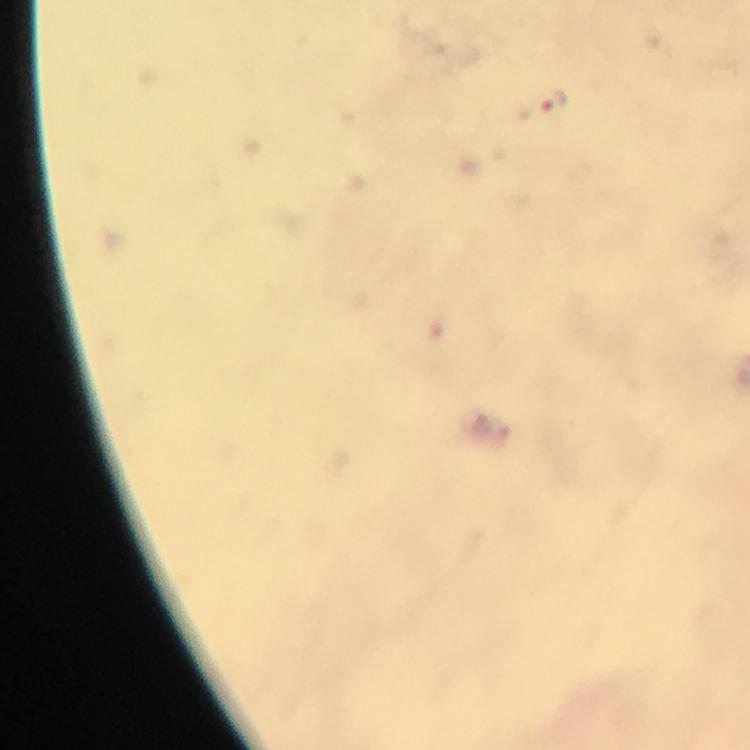
Approximate centers as {x, y} in pixels.
Summary:
  - Malaria parasite locations: {541, 102}
  - Stain: Giemsa
  - Preparation: thick smear
  - Immersion oil: applied
  - Context: from a malaria diagnostic workup
  - Capture: smartphone camera through the microscope
  - Cropped from: one field of view
  - Magnification: 100x
  - Image size: 750×750 pixels